Assess for malaria.
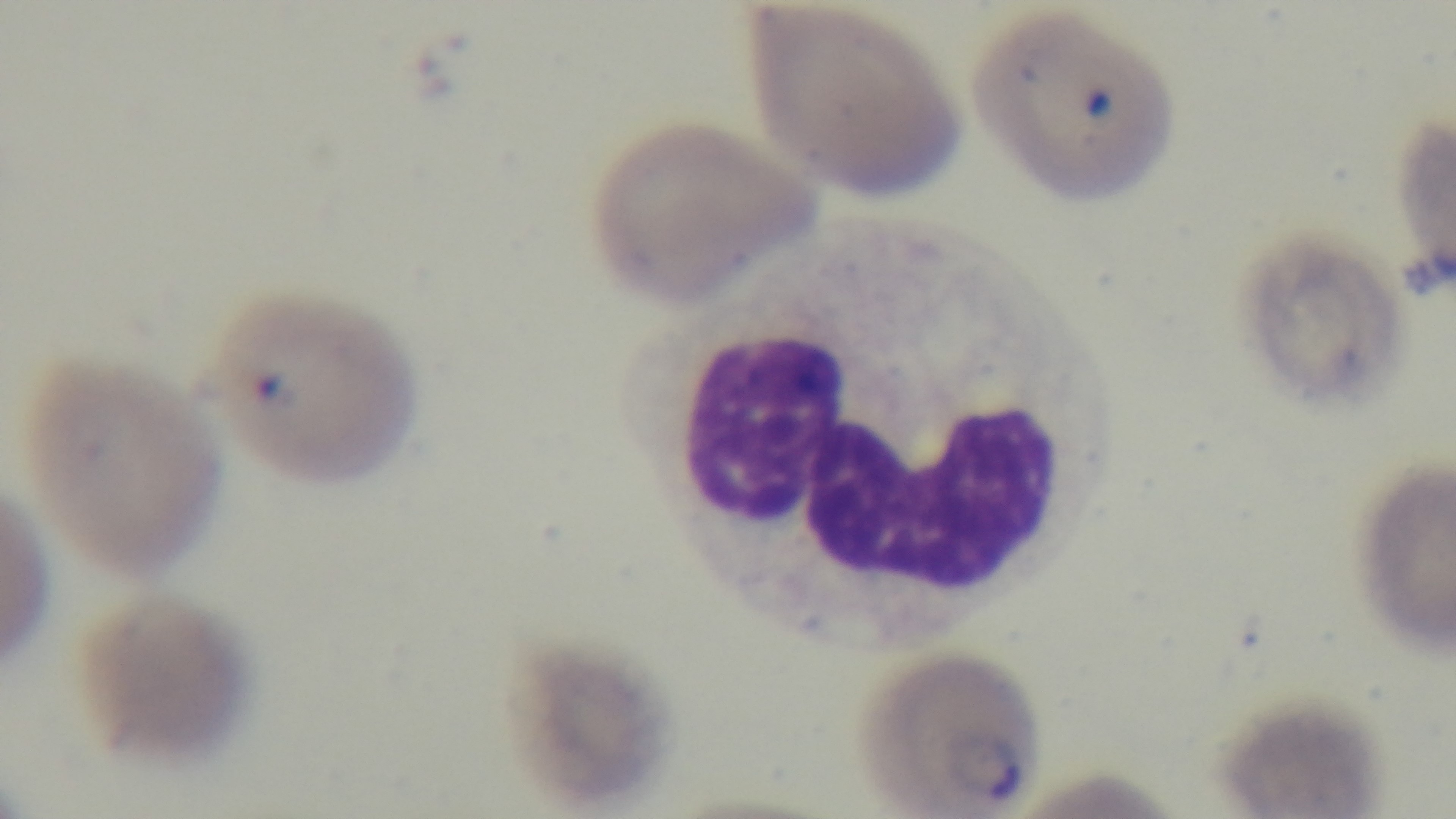

Positive.

preparation = thin blood film
modality = light microscopy
capture = mounted 4K digital camera
field of view = one from the slide
stain = Giemsa
objective = 100x oil immersion